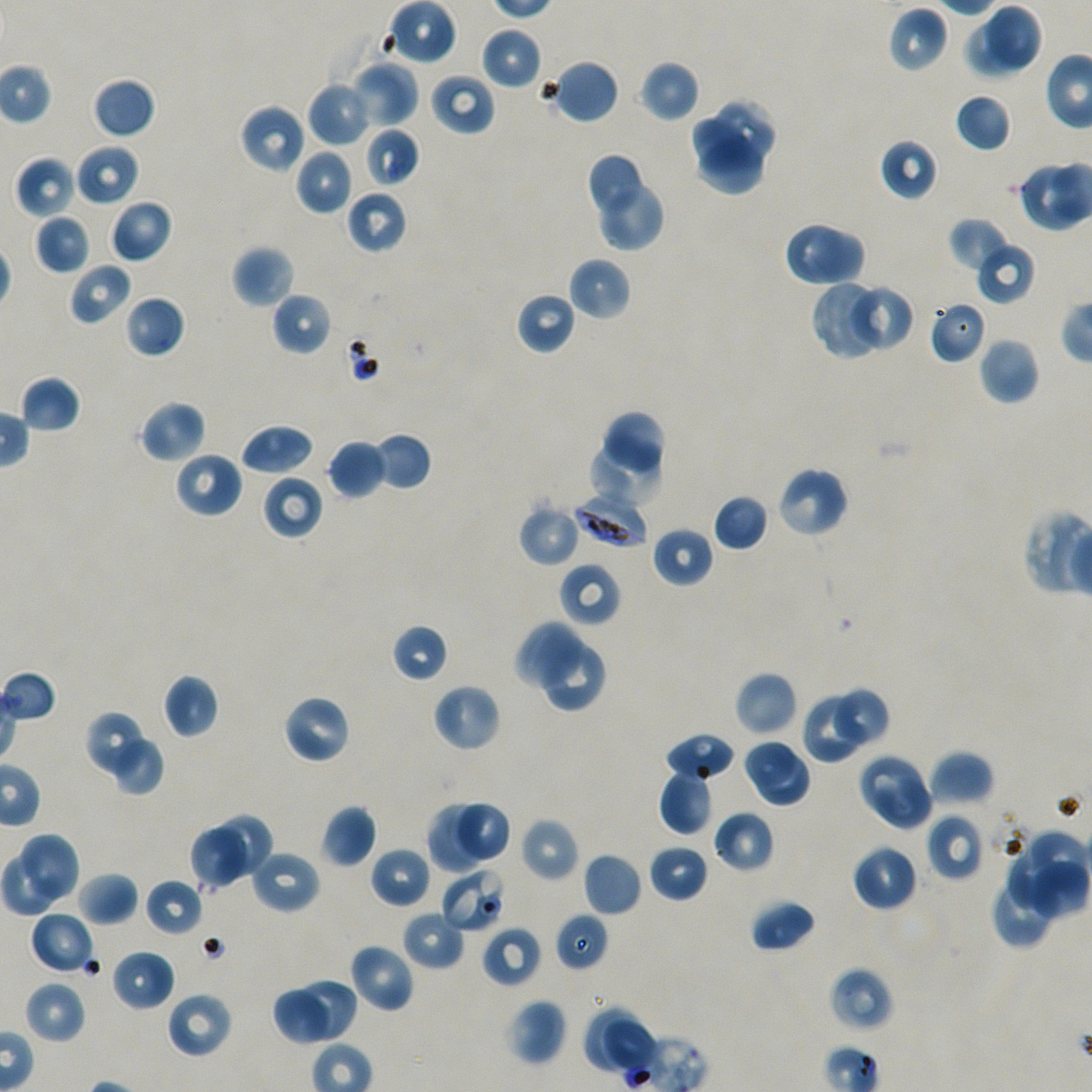

Not every red blood cell is marked.
preparation = thin blood smear
locations of red blood cells of indeterminate infection status = approximate bounding boxes as (x1, y1, x2, y2) in pixels: (440, 868, 507, 933)
locations of uninfected red blood cells = approximate bounding boxes as (x1, y1, x2, y2) in pixels: (386, 0, 457, 65), (888, 5, 948, 73), (987, 5, 1043, 70), (964, 22, 1033, 77), (480, 26, 542, 90), (549, 58, 620, 125), (349, 60, 419, 128), (638, 60, 701, 122), (429, 72, 496, 136), (92, 77, 156, 139), (308, 80, 374, 147), (954, 92, 1012, 153), (715, 98, 777, 164), (239, 103, 308, 173), (687, 115, 751, 170), (365, 128, 420, 187), (696, 134, 765, 198), (879, 139, 939, 201), (75, 145, 139, 205), (294, 148, 354, 216), (585, 153, 644, 217), (14, 156, 76, 219), (1015, 161, 1085, 232), (597, 185, 666, 251), (346, 189, 407, 255), (109, 200, 173, 263), (34, 213, 92, 275), (949, 216, 1012, 272), (784, 221, 867, 288), (976, 242, 1036, 305), (232, 244, 295, 309), (568, 257, 632, 321), (68, 262, 132, 326), (810, 280, 887, 360), (845, 283, 914, 353), (272, 291, 332, 357), (514, 291, 576, 356), (124, 295, 185, 359), (928, 299, 988, 364), (978, 337, 1040, 405), (20, 374, 82, 433), (139, 400, 206, 464), (604, 410, 668, 473), (241, 424, 314, 476), (371, 432, 432, 491), (327, 439, 386, 499), (587, 440, 667, 502), (173, 450, 244, 519), (776, 466, 848, 539), (262, 473, 324, 540), (712, 493, 769, 551), (517, 503, 581, 567), (651, 526, 713, 588), (558, 561, 621, 627), (515, 623, 586, 693), (391, 624, 449, 683), (539, 645, 606, 712), (734, 671, 798, 737), (162, 673, 219, 740), (432, 682, 501, 752), (835, 685, 892, 747), (801, 693, 867, 764), (283, 695, 352, 764), (84, 710, 145, 776), (663, 733, 737, 782), (114, 739, 165, 795), (742, 739, 802, 794), (928, 750, 994, 807), (856, 752, 927, 820), (758, 754, 813, 812), (659, 770, 714, 836), (875, 777, 935, 832), (427, 802, 484, 873), (456, 803, 513, 864), (321, 805, 377, 868), (712, 809, 775, 873), (216, 814, 272, 880), (926, 814, 985, 881), (520, 817, 580, 882), (188, 826, 251, 890), (1019, 829, 1088, 890), (19, 833, 80, 903), (648, 844, 708, 903), (851, 844, 918, 911), (369, 847, 432, 909), (249, 849, 321, 915), (1, 852, 60, 922), (582, 852, 642, 917), (1007, 852, 1059, 911), (1027, 861, 1089, 920), (76, 871, 139, 926), (991, 876, 1052, 950), (145, 878, 204, 936), (749, 898, 816, 953), (29, 910, 95, 975), (402, 911, 465, 970), (553, 913, 609, 972), (481, 925, 543, 989), (349, 942, 416, 1014), (111, 949, 176, 1011), (829, 966, 894, 1032), (294, 977, 358, 1042), (23, 980, 87, 1044), (274, 987, 331, 1046), (166, 991, 233, 1059), (505, 998, 568, 1066), (583, 1006, 647, 1078)
locations of infected red blood cells = approximate bounding boxes as (x1, y1, x2, y2) in pixels: (575, 494, 647, 546)
stain = Giemsa
image size = 1092×1092 pixels
field of view = one from this slide
objective = 100x, oil immersion, numerical aperture 1.45
donor blood group = A+/O+
culture = in-vitro Plasmodium falciparum strain NF54, static